Report the malaria status.
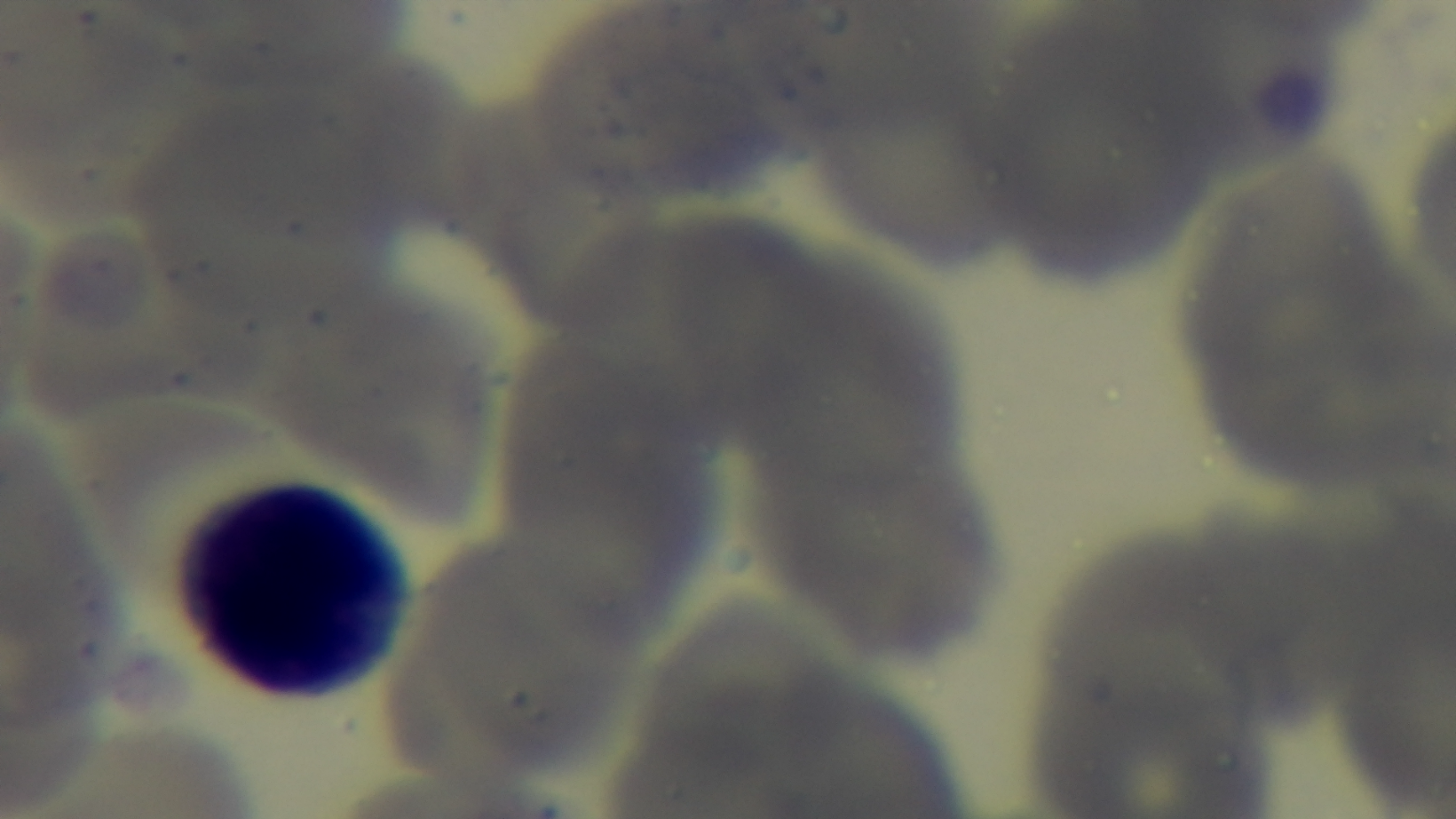

It is uninfected.

{
  "capture": "mounted 4K digital camera",
  "preparation": "thin",
  "objective": "100x oil immersion",
  "modality": "light microscopy",
  "stain": "Giemsa",
  "field_of_view": "single"
}